Classify this cell by malaria status.
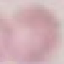
It is uninfected.

Thin blood smear. Giemsa-stained preparation. Automatically extracted cell patch, resized to 64 × 64 pixels. Photographed with a smartphone camera at the microscope eyepiece.